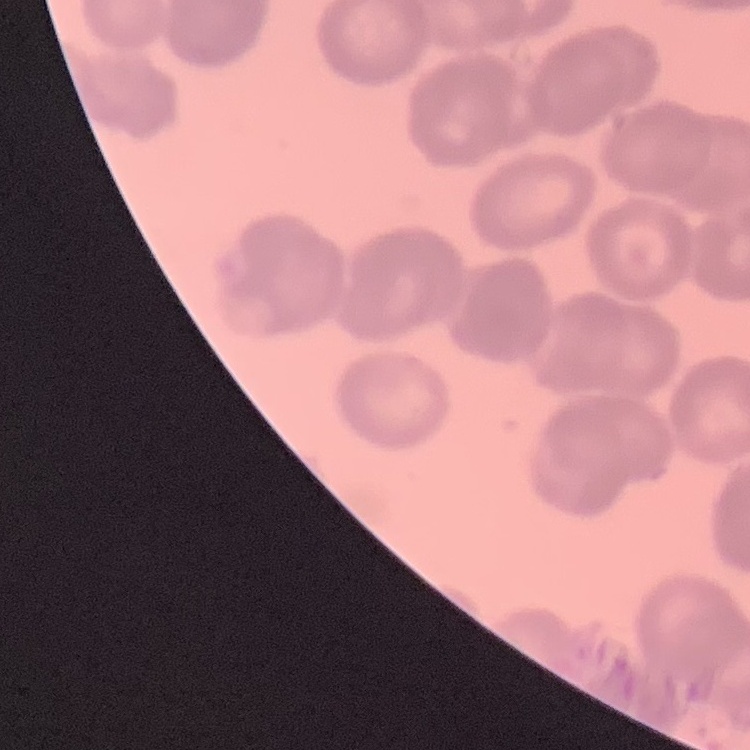
red blood cell morphology = rouleaux formation
preparation = thin blood film
stain = Field's or Giemsa
image type = one tile cut from a larger photomicrograph